Assess this cell for malaria.
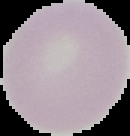

It is uninfected.

image size = 130×136 pixels
image type = segmented cell region with the area outside set to black
preparation = thin blood smear